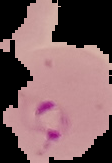

Summary:
  - Preparation: thin blood smear
  - Image type: cell region segmented out of the field of view; surrounding area masked to black
  - Result: Plasmodium parasites identified
  - Image size: 112×163 pixels